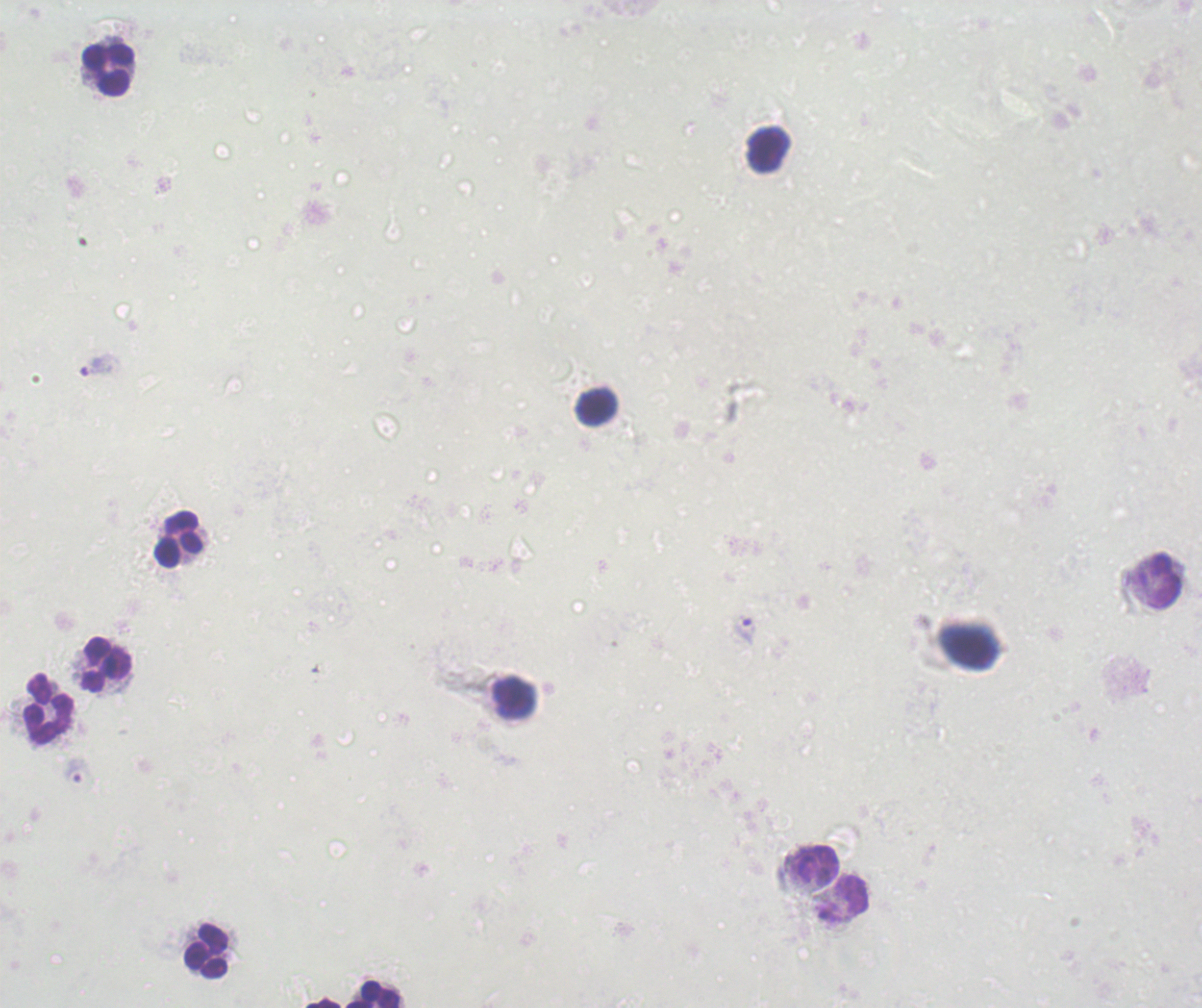
Approximate centers as {x, y} in pixels.
Summary:
  - Leukocyte locations: {107, 70}, {768, 150}, {598, 408}, {178, 538}, {1158, 581}, {106, 664}, {513, 697}, {49, 708}, {815, 863}, {844, 899}, {206, 949}, {371, 995}, {322, 1003}
  - Trophozoite locations: {100, 364}, {745, 631}
  - Magnification: 100x
  - Background quality: poor
  - Preparation: thick blood smear
  - Field of view: single
  - Context: previously used in an actual diagnosis
  - Image size: 1202×1008 pixels
  - Stain: Romanowsky
  - Result: positive for Plasmodium parasites